Assess the morphology of the red blood cells.
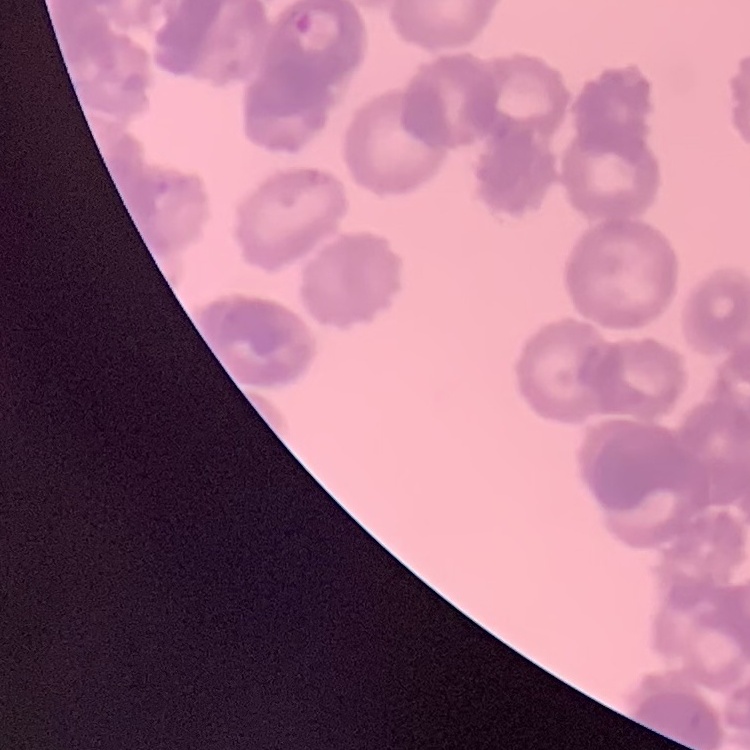

Rouleaux formation.

Square crop of a larger photomicrograph. Field's or Giemsa stain. Thin blood smear.